Name the parasite shown.
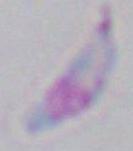
This is Toxoplasma gondii.

{
  "modality": "photomicrograph",
  "magnification": "1000x"
}